Assess this cell for malaria.
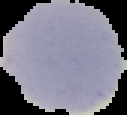

Uninfected.

Image is 127×115 pixels. From a thin blood film. Segmented cell region on a black background.